Identify the preparation type.
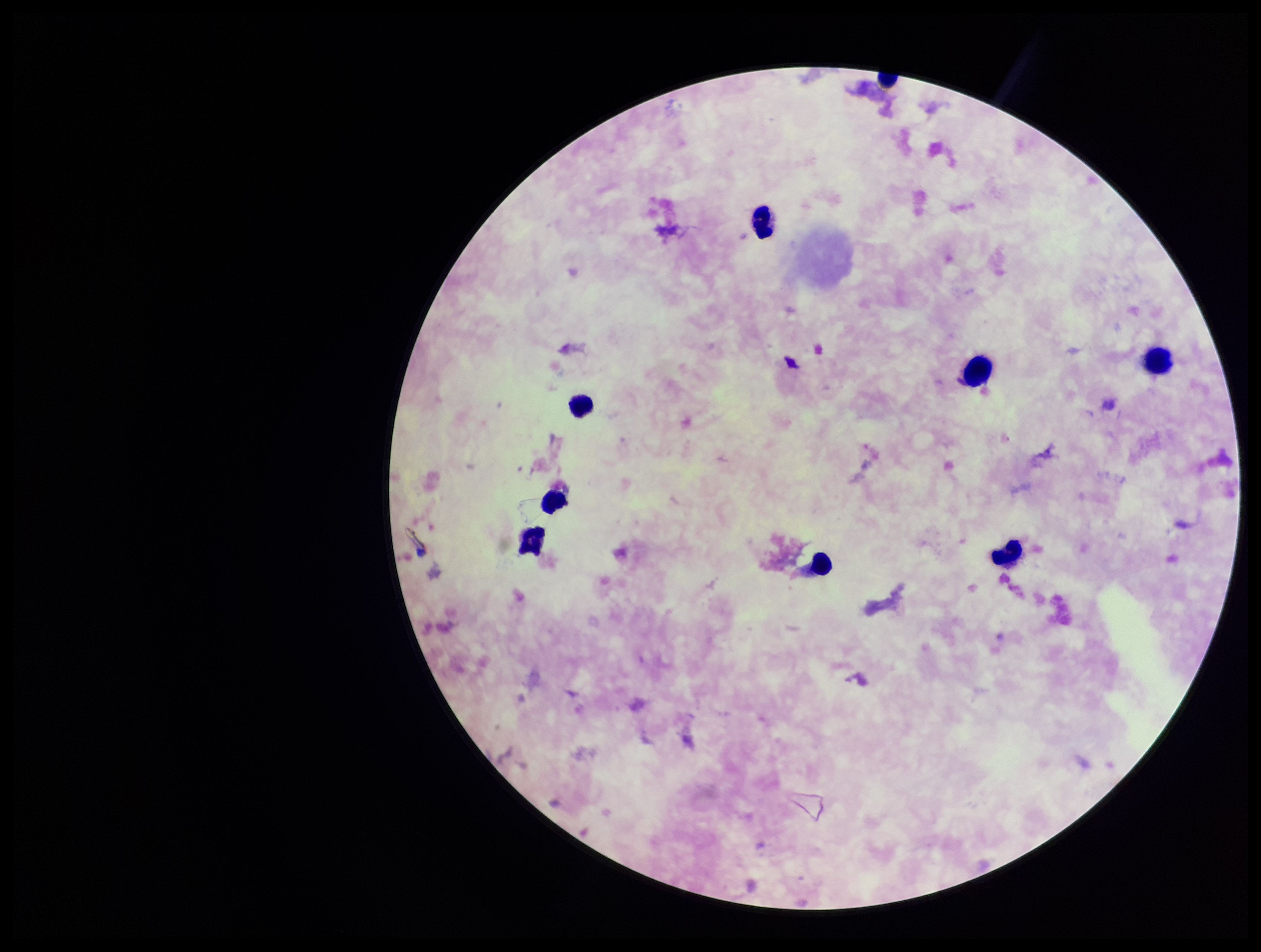

Thick.

field of view = single
parasite count = 0
stain = Giemsa
image size = 1261×952 pixels
patient malaria status = positive
leukocyte count = 9
capture = smartphone photograph through the microscope eyepiece
species reported for this patient = Plasmodium falciparum
Plasmodium parasites = none seen